Draw a bounding box around every leukocyte (white blood cell).
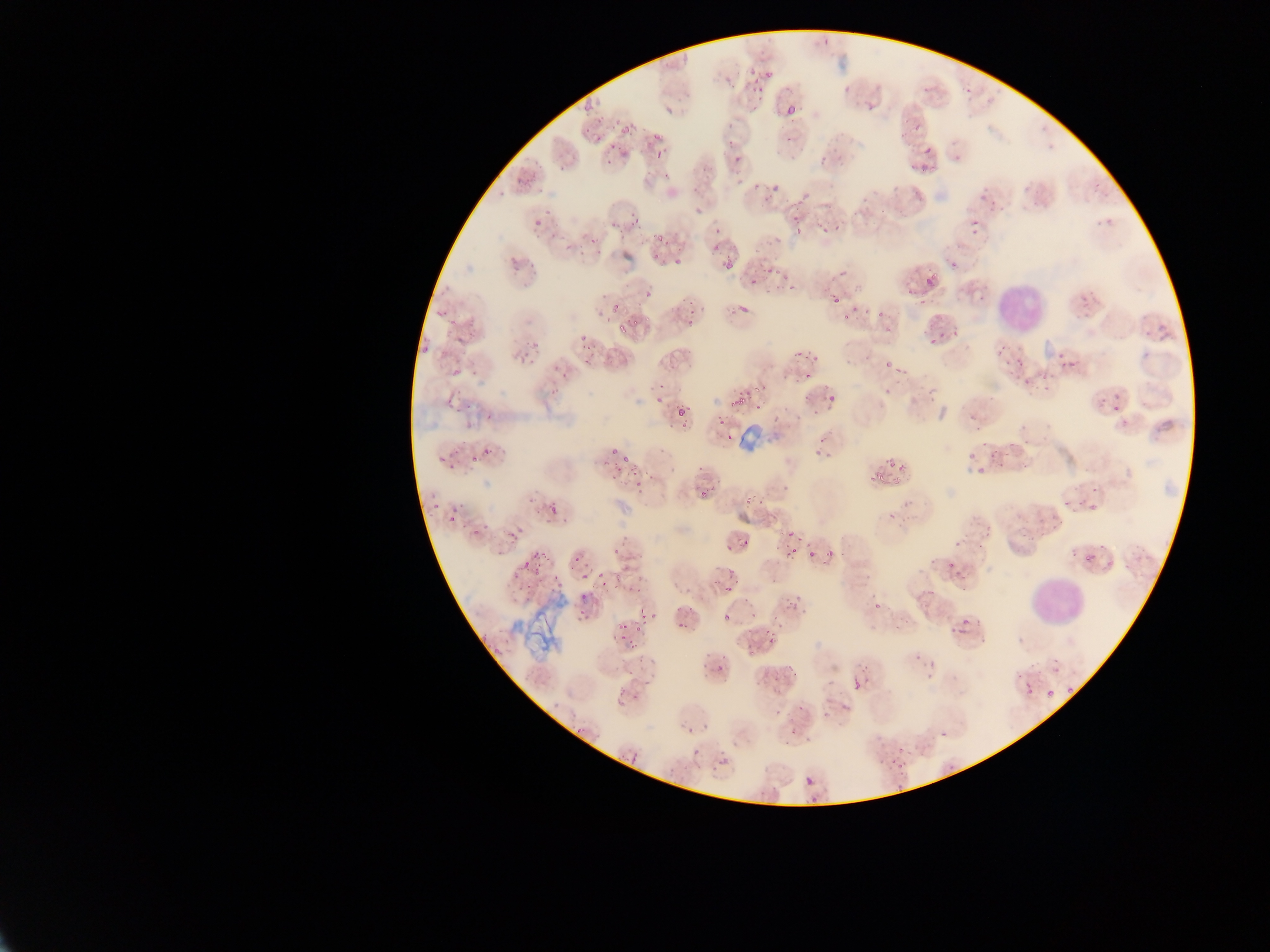

Approximate bounding boxes as [left, top, right, bottom] in pixels.
Leukocytes: [979, 279, 1040, 342], [1025, 560, 1080, 626].

preparation = thin blood smear
Plasmodium parasite locations = approximate bounding boxes as [left, top, right, bottom] in pixels: [753, 50, 773, 78], [724, 69, 736, 81], [953, 76, 981, 104], [746, 78, 764, 98], [784, 99, 800, 118], [665, 106, 675, 117], [722, 113, 743, 135], [618, 118, 635, 141], [914, 118, 930, 132], [646, 123, 660, 144], [721, 139, 742, 160], [597, 141, 609, 160], [649, 142, 662, 163], [920, 142, 952, 174], [613, 147, 630, 160], [732, 157, 751, 178], [767, 174, 788, 198], [515, 177, 526, 186], [536, 183, 545, 195], [751, 184, 759, 194], [627, 204, 637, 227], [780, 204, 805, 236], [689, 205, 700, 215], [517, 212, 544, 226], [612, 213, 625, 230], [966, 213, 990, 240], [813, 220, 835, 243], [564, 226, 574, 239], [707, 228, 725, 253], [656, 234, 666, 242], [577, 239, 602, 259], [720, 254, 737, 279], [662, 255, 682, 272], [949, 260, 958, 269], [833, 262, 850, 285], [760, 263, 775, 286], [786, 277, 798, 296], [906, 278, 922, 295], [922, 278, 939, 293], [597, 286, 608, 300], [640, 288, 654, 296], [733, 293, 756, 312], [832, 295, 842, 304], [838, 297, 875, 327], [446, 300, 454, 319], [433, 304, 439, 322], [610, 304, 620, 314], [684, 308, 700, 324], [875, 309, 885, 318], [615, 317, 629, 334], [929, 317, 948, 345], [1151, 317, 1177, 340], [461, 326, 479, 343], [575, 332, 584, 347], [419, 339, 432, 356], [1002, 345, 1024, 371], [1057, 348, 1069, 371], [522, 352, 536, 364], [581, 353, 593, 364], [799, 354, 816, 386], [884, 360, 892, 369], [450, 368, 461, 378], [1017, 369, 1045, 384], [894, 370, 906, 390], [560, 371, 572, 381], [929, 379, 948, 398], [732, 381, 760, 406], [650, 385, 664, 409], [821, 385, 839, 409], [801, 394, 813, 411], [1113, 400, 1127, 419], [1095, 402, 1106, 414], [674, 405, 684, 415], [974, 409, 986, 423], [482, 410, 494, 423], [710, 416, 724, 435], [1028, 421, 1038, 433], [661, 431, 669, 436], [815, 436, 832, 460], [1003, 441, 1018, 464], [981, 443, 996, 458], [481, 444, 500, 460], [605, 444, 618, 452], [471, 449, 485, 466], [435, 450, 447, 465], [450, 453, 464, 478], [609, 457, 630, 485], [888, 459, 900, 470], [863, 467, 884, 486], [968, 469, 979, 479], [635, 479, 645, 495], [1075, 481, 1099, 508], [746, 487, 756, 508], [782, 487, 792, 499], [421, 488, 442, 511], [698, 490, 712, 502], [544, 502, 558, 515], [442, 505, 456, 524], [884, 514, 900, 528], [1043, 518, 1053, 526], [507, 522, 521, 545], [470, 526, 483, 547], [785, 529, 794, 538], [737, 532, 752, 546], [539, 545, 554, 566], [722, 545, 731, 557], [775, 545, 784, 556], [783, 546, 800, 561], [826, 549, 835, 557], [807, 550, 816, 558], [570, 551, 582, 565], [952, 551, 964, 565], [520, 553, 536, 567], [577, 566, 590, 578], [593, 566, 612, 580], [524, 570, 540, 583], [550, 572, 565, 594], [717, 573, 738, 595], [631, 580, 646, 597], [921, 580, 935, 597], [783, 589, 800, 618], [580, 592, 592, 609], [869, 602, 875, 614], [750, 603, 761, 621], [770, 610, 786, 624], [723, 611, 731, 621], [616, 613, 629, 632], [635, 615, 649, 628], [949, 617, 971, 636], [676, 622, 687, 635], [765, 631, 775, 646], [629, 637, 643, 651], [742, 640, 752, 654], [701, 647, 715, 666], [919, 651, 944, 674], [785, 660, 800, 683], [628, 662, 642, 678], [714, 664, 724, 678], [845, 664, 859, 694], [1053, 665, 1063, 675], [770, 672, 782, 689], [1021, 680, 1033, 693], [1065, 683, 1074, 693], [1044, 688, 1054, 700], [634, 689, 646, 700], [792, 702, 806, 716], [685, 724, 699, 739], [781, 730, 798, 742], [884, 746, 896, 769], [897, 754, 913, 770], [716, 756, 727, 767], [805, 777, 814, 786], [879, 780, 909, 787], [808, 791, 818, 801] | approximate [x, y] pixel centers of objects too small to bound: [690, 605], [943, 734]
image size = 1270×952 pixels
capture = mobile-phone photograph through a microscope
country = Ghana
field of view = single
artifact (stain precipitate or debris) locations = approximate bounding boxes as [left, top, right, bottom] in pixels: [513, 602, 574, 660]